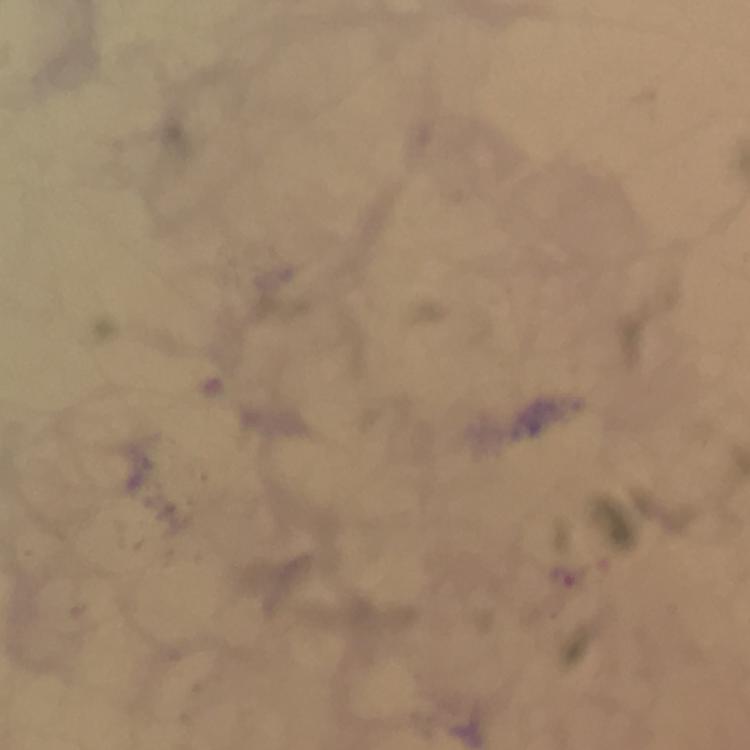
Approximate centers as [x, y] in pixels. Malaria parasite locations: [563, 577]. Photographed with a smartphone mounted on the microscope. At 100x magnification. Cropped region of a single field of view. Image is 750×750 pixels. From a diagnostic examination for malaria. Immersion oil was used. Giemsa-stained preparation. Thick blood smear.